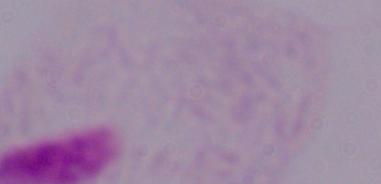

Summary:
  - Identification: trichomonad
  - Magnification: 1000x
  - Modality: photomicrograph